Outline each blood parasite and name the species.
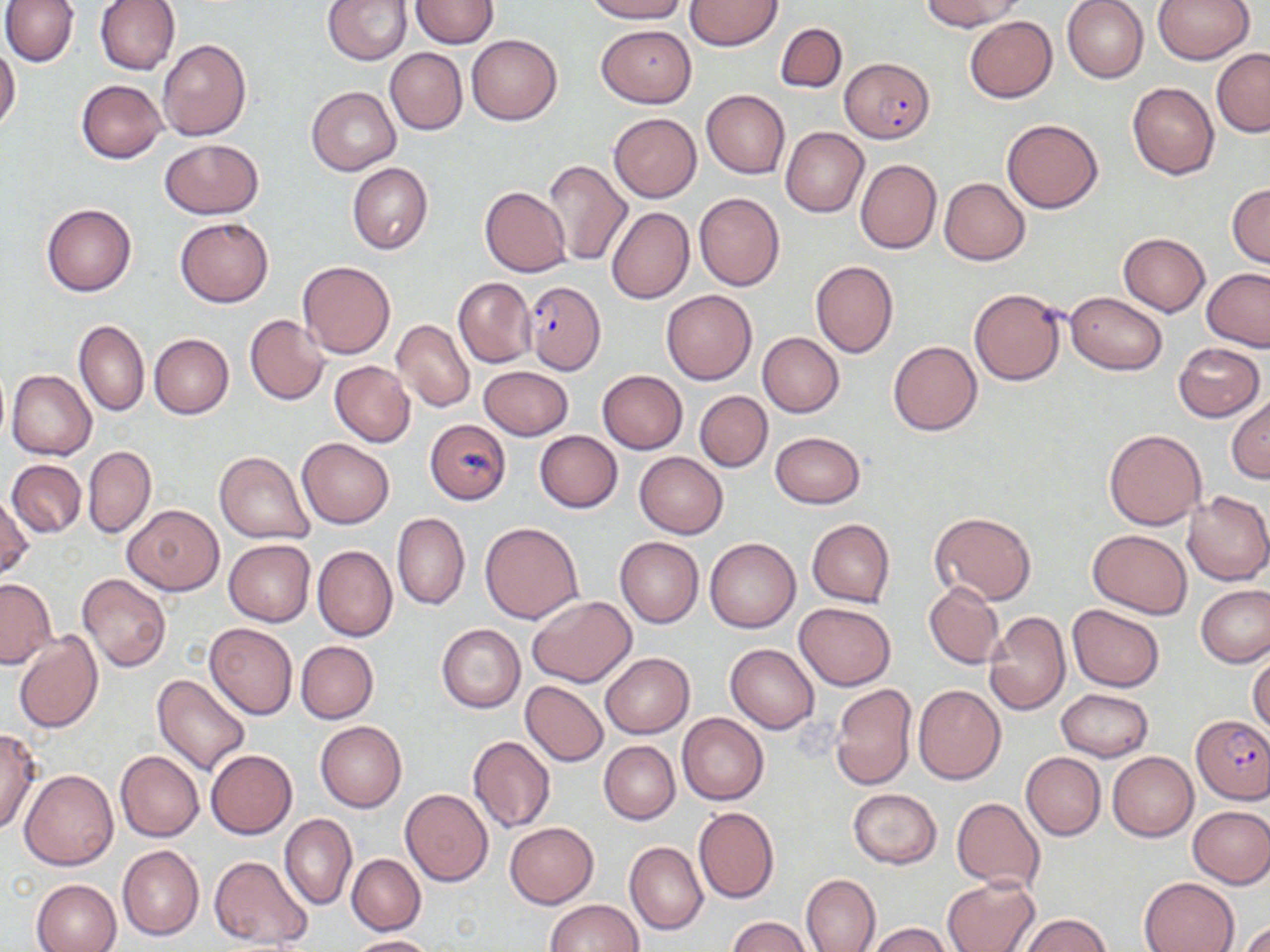
Approximate bounding boxes as (x1,y1)-(x2,y2) corner pairs in pixels.
Plasmodium falciparum-infected red blood cells: (839,57)-(935,143), (521,280)-(605,374), (1191,715)-(1270,802).
No Plasmodium ovale, Plasmodium malariae, Plasmodium vivax, Babesia divergens, or Trypanosoma brucei observed.

Uninfected red blood cell locations: (1,0)-(80,67), (95,0)-(179,75), (323,0)-(412,65), (411,0)-(499,48), (586,0)-(686,23), (685,0)-(781,50), (921,0)-(1026,30), (1062,0)-(1149,83), (1152,0)-(1254,64), (964,16)-(1057,103), (596,24)-(696,107), (775,24)-(847,93), (466,34)-(561,125), (156,39)-(251,141), (0,46)-(20,134), (385,48)-(466,135), (1212,48)-(1270,137), (76,80)-(168,164), (1127,82)-(1219,179), (306,86)-(400,176), (701,89)-(790,179), (608,114)-(701,202), (1002,117)-(1104,213), (781,127)-(868,217), (159,137)-(263,219), (542,158)-(630,266), (855,159)-(941,255), (348,162)-(432,254), (938,176)-(1030,265), (1227,183)-(1269,268), (480,186)-(572,278), (694,193)-(785,291), (42,203)-(137,296), (606,207)-(694,303), (175,217)-(273,307), (1118,233)-(1209,316), (1078,252)-(1201,368), (297,261)-(395,359), (811,261)-(898,358), (1201,268)-(1270,351), (453,277)-(536,367), (968,289)-(1065,384), (661,290)-(756,384), (1065,293)-(1166,374), (245,314)-(330,406), (75,320)-(149,417), (392,320)-(475,413), (757,332)-(844,417), (149,334)-(234,419), (888,340)-(983,435), (1174,342)-(1264,421), (329,361)-(416,447), (479,366)-(573,440), (7,369)-(96,462), (596,370)-(687,453), (695,391)-(772,471), (1227,397)-(1270,482), (424,420)-(511,504), (1104,428)-(1208,530), (534,431)-(623,513), (770,431)-(866,509), (296,437)-(394,528), (83,446)-(156,538), (215,451)-(314,543), (634,452)-(728,539), (7,459)-(86,537), (1183,491)-(1270,586), (0,492)-(32,581), (123,503)-(223,596), (929,511)-(1036,605), (393,512)-(470,610), (807,518)-(895,606), (481,521)-(584,625), (1088,529)-(1192,617), (614,536)-(704,628), (704,537)-(800,633), (224,540)-(315,626), (312,545)-(397,641), (77,574)-(170,673), (0,579)-(56,668), (924,582)-(1004,668), (1195,584)-(1270,667), (527,595)-(635,687), (794,602)-(895,691), (1068,605)-(1163,691), (984,612)-(1070,715), (204,622)-(298,719), (436,624)-(525,714), (14,631)-(103,732), (296,641)-(379,723), (725,643)-(819,733), (1248,652)-(1270,737), (601,654)-(694,737), (152,674)-(250,777), (520,681)-(609,766), (831,684)-(917,790), (913,685)-(1005,784), (1057,689)-(1153,761), (677,713)-(768,805), (315,720)-(406,812), (0,729)-(41,836), (468,735)-(555,833), (599,741)-(679,824), (205,749)-(297,838), (116,750)-(203,842), (1021,751)-(1105,840), (1108,752)-(1198,841), (20,770)-(119,871), (847,788)-(942,869), (401,789)-(493,886), (953,797)-(1045,892), (1188,805)-(1270,889), (693,807)-(779,904), (280,813)-(356,911), (505,822)-(599,908), (626,842)-(708,934), (118,844)-(203,940), (347,853)-(425,935), (209,855)-(313,948), (800,874)-(880,952), (943,875)-(1039,952), (1138,877)-(1239,952), (31,879)-(120,952), (546,899)-(644,952), (1023,914)-(1112,951), (729,916)-(810,952), (1237,919)-(1270,952), (869,923)-(955,952), (345,935)-(434,952). Slide-level diagnosis: Plasmodium falciparum. May-Grünwald-Giemsa-stained preparation. Image is 1270×952 pixels. Thin blood smear. One field of a larger specimen. Captured at 1000x magnification. Optical microscopy.